Name the parasite shown.
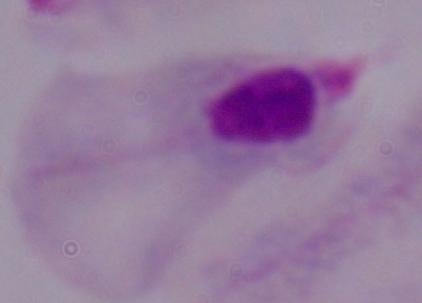
This is a trichomonad.

1000x magnification. Photomicrograph.